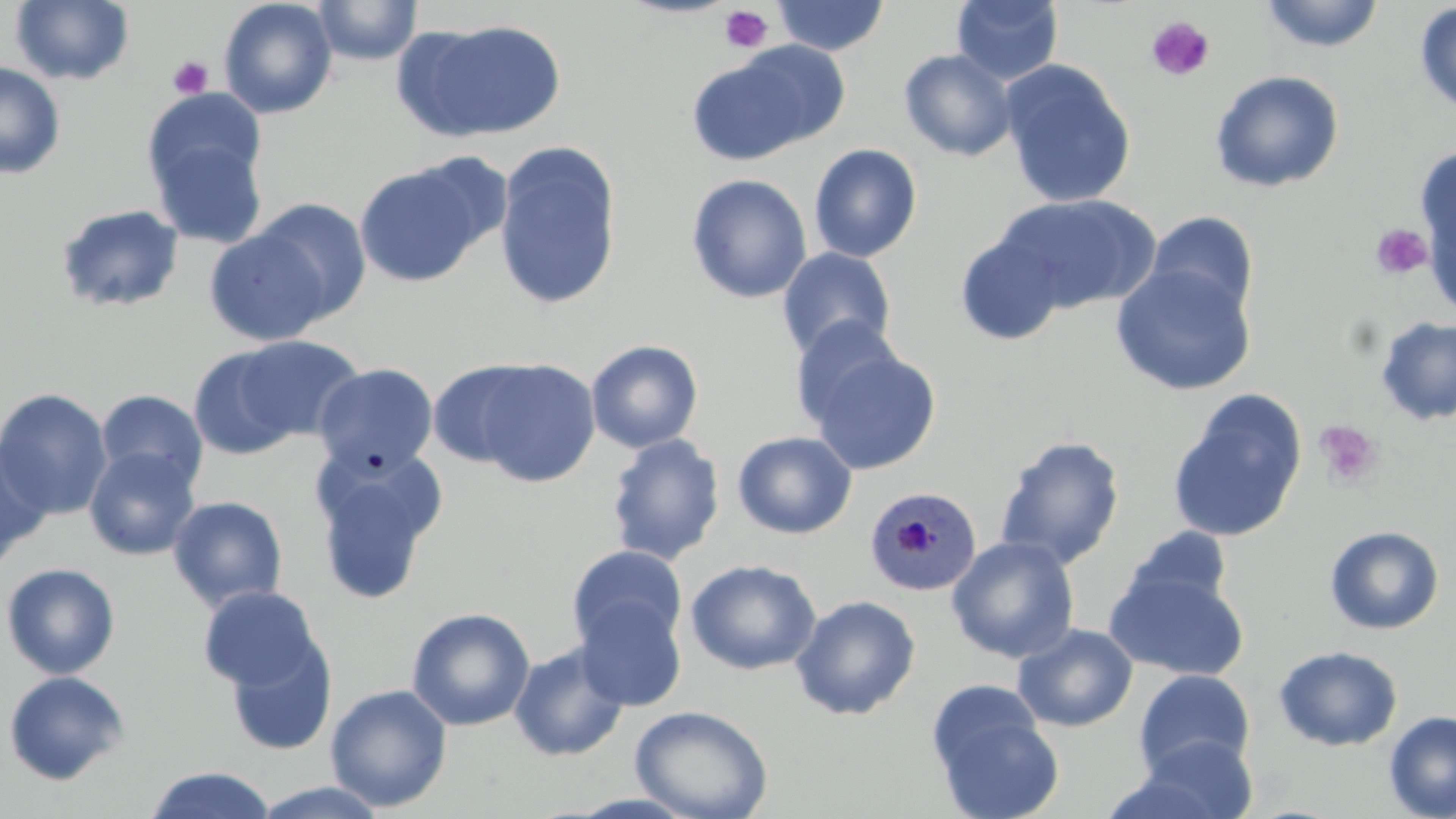

Approximate bounding boxes as named x1/y1/x2/y2 corners in pixels. Uninfected red blood cell locations: (x1=10, y1=0, x2=134, y2=85), (x1=218, y1=0, x2=338, y2=119), (x1=313, y1=0, x2=422, y2=66), (x1=772, y1=0, x2=889, y2=56), (x1=951, y1=0, x2=1064, y2=86), (x1=1258, y1=0, x2=1386, y2=53), (x1=1414, y1=2, x2=1456, y2=119), (x1=410, y1=18, x2=567, y2=140), (x1=731, y1=40, x2=854, y2=149), (x1=898, y1=48, x2=1019, y2=161), (x1=686, y1=54, x2=816, y2=165), (x1=999, y1=60, x2=1137, y2=208), (x1=0, y1=62, x2=66, y2=179), (x1=1209, y1=69, x2=1345, y2=193), (x1=144, y1=103, x2=269, y2=245), (x1=493, y1=142, x2=623, y2=311), (x1=808, y1=143, x2=923, y2=263), (x1=1415, y1=144, x2=1455, y2=289), (x1=353, y1=158, x2=492, y2=289), (x1=685, y1=173, x2=812, y2=304), (x1=995, y1=193, x2=1159, y2=314), (x1=248, y1=198, x2=373, y2=324), (x1=55, y1=203, x2=186, y2=313), (x1=1144, y1=211, x2=1260, y2=322), (x1=203, y1=226, x2=334, y2=345), (x1=955, y1=229, x2=1070, y2=346), (x1=776, y1=247, x2=897, y2=361), (x1=1110, y1=264, x2=1257, y2=395), (x1=1374, y1=315, x2=1456, y2=426), (x1=789, y1=317, x2=905, y2=430), (x1=229, y1=335, x2=367, y2=443), (x1=585, y1=339, x2=704, y2=454), (x1=805, y1=345, x2=942, y2=475), (x1=188, y1=346, x2=306, y2=461), (x1=466, y1=358, x2=602, y2=488), (x1=427, y1=360, x2=545, y2=470), (x1=312, y1=363, x2=438, y2=477), (x1=0, y1=387, x2=113, y2=520), (x1=95, y1=388, x2=209, y2=493), (x1=1166, y1=390, x2=1308, y2=544), (x1=732, y1=431, x2=858, y2=540), (x1=605, y1=433, x2=725, y2=565), (x1=994, y1=435, x2=1126, y2=570), (x1=0, y1=440, x2=52, y2=567), (x1=83, y1=446, x2=201, y2=561), (x1=310, y1=447, x2=446, y2=604), (x1=167, y1=495, x2=289, y2=612), (x1=1324, y1=525, x2=1445, y2=635), (x1=1121, y1=526, x2=1234, y2=617), (x1=946, y1=535, x2=1080, y2=664), (x1=567, y1=545, x2=688, y2=655), (x1=685, y1=559, x2=821, y2=676), (x1=1, y1=562, x2=121, y2=680), (x1=1105, y1=567, x2=1250, y2=681), (x1=197, y1=585, x2=326, y2=693), (x1=791, y1=594, x2=921, y2=720), (x1=574, y1=596, x2=687, y2=712), (x1=406, y1=606, x2=536, y2=731), (x1=1012, y1=623, x2=1138, y2=732), (x1=224, y1=631, x2=338, y2=757), (x1=508, y1=641, x2=630, y2=762), (x1=1273, y1=645, x2=1403, y2=751), (x1=1133, y1=668, x2=1255, y2=779), (x1=1, y1=670, x2=131, y2=785), (x1=325, y1=683, x2=453, y2=813), (x1=926, y1=686, x2=1065, y2=819), (x1=629, y1=704, x2=774, y2=818), (x1=1383, y1=710, x2=1456, y2=819), (x1=1124, y1=734, x2=1259, y2=819), (x1=143, y1=766, x2=277, y2=819), (x1=250, y1=781, x2=391, y2=818). Plasmodium malariae-infected red blood cell locations: (x1=863, y1=485, x2=982, y2=598). Platelet locations: (x1=718, y1=5, x2=773, y2=53), (x1=1145, y1=15, x2=1215, y2=82), (x1=168, y1=55, x2=213, y2=99), (x1=1369, y1=223, x2=1434, y2=281), (x1=1314, y1=420, x2=1384, y2=490). Slide-level diagnosis: Plasmodium malariae. Thin blood film. Light microscopy. Single field of view. Image is 1456×819 pixels. May-Grünwald-Giemsa-stained preparation. Captured at 1000x magnification.